State which parasite is depicted.
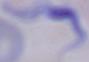
This is a trypanosome.

Summary:
  - Modality: micrograph
  - Magnification: 1000x